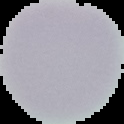

The area outside the segmented cell region is set to black. From a thin blood smear. Result: no Plasmodium parasites seen. Image is 124×124 pixels.